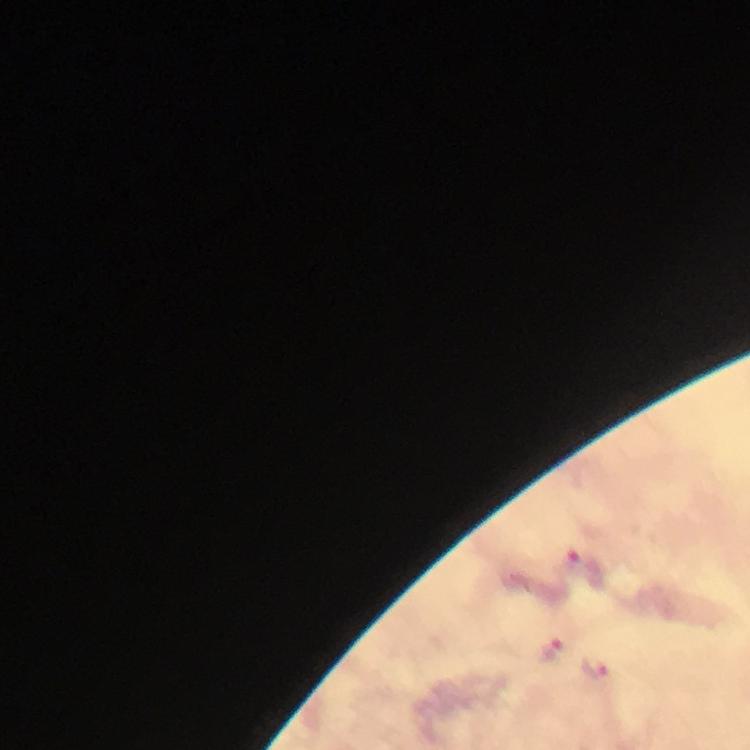 Approximate centers as (x, y) in pixels. Malaria parasite locations: (551, 650), (596, 667). Immersion oil was used. Image is 750×750 pixels. Photographed through the microscope with a smartphone camera. 100x magnification. Giemsa stain. Cropped region of a single field of view. Thick smear. From a diagnostic examination for malaria.